Identify the blood parasite species.
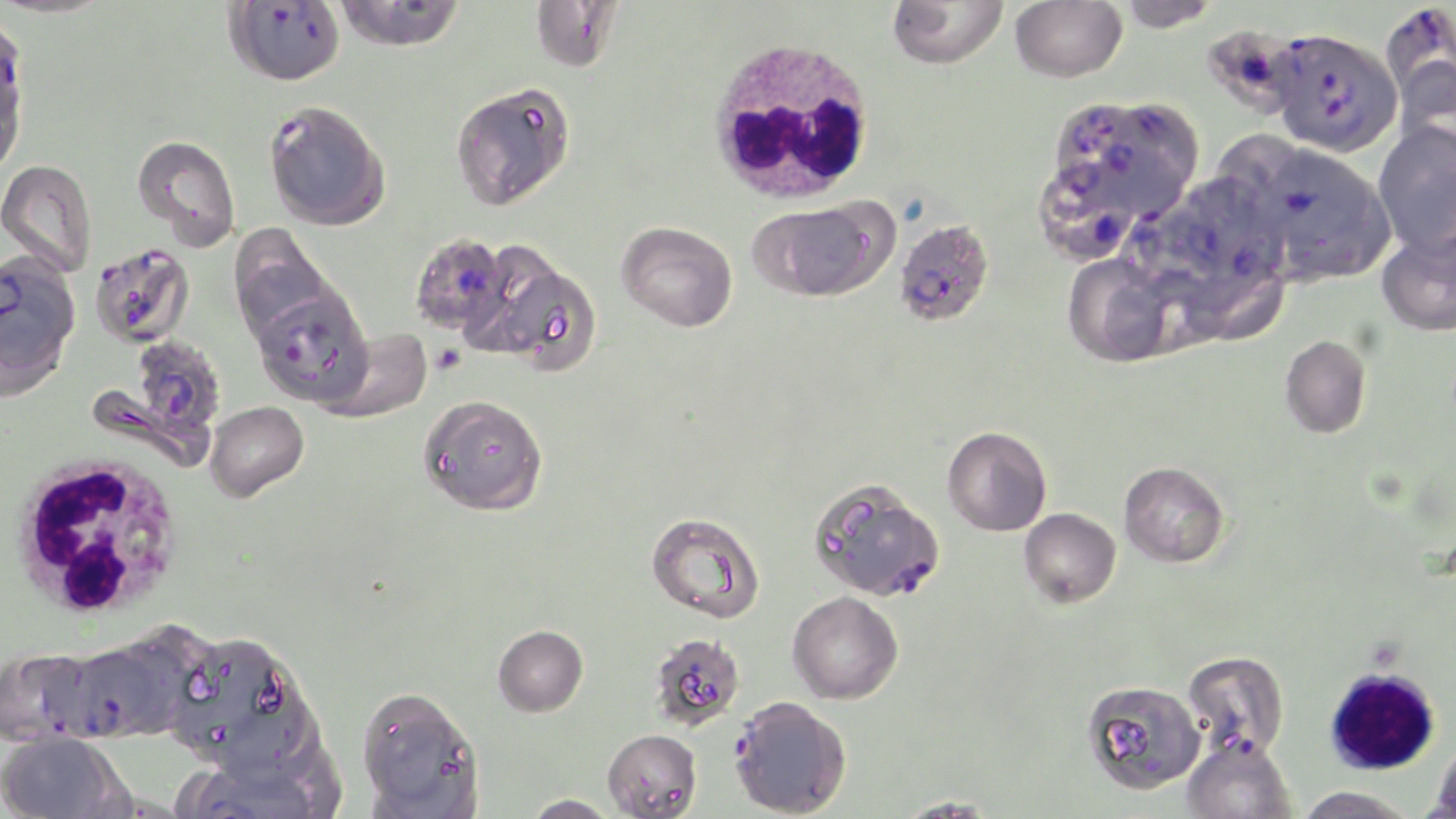
Plasmodium falciparum.

Approximate bounding boxes as (x1,y1)-(x2,y2) corner pairs in pixels. Plasmodium falciparum-infected red blood cell locations: (224,1)-(347,87), (1381,3)-(1456,128), (1201,24)-(1305,120), (1269,28)-(1402,157), (0,30)-(30,126), (1103,97)-(1207,189), (1054,99)-(1161,206), (263,100)-(390,231), (1266,150)-(1372,244), (1120,206)-(1222,302), (893,218)-(993,326), (409,232)-(512,336), (89,243)-(195,348), (0,253)-(81,394), (250,285)-(373,409), (128,337)-(227,443), (810,479)-(946,602), (63,642)-(177,742), (0,647)-(103,747), (1181,650)-(1289,759), (728,695)-(852,817). Platelet locations: (431,345)-(466,374). Uninfected red blood cell locations: (332,0)-(466,53), (531,0)-(624,72), (887,0)-(1009,70), (1010,0)-(1127,82), (1116,0)-(1221,31), (451,81)-(576,208), (1372,121)-(1456,255), (1220,129)-(1291,204), (132,134)-(241,251), (0,159)-(97,276), (751,201)-(886,299), (617,221)-(738,332), (229,224)-(334,342), (1376,226)-(1455,336), (1062,252)-(1179,367), (488,260)-(603,378), (1187,275)-(1297,350), (321,328)-(433,423), (1280,334)-(1372,438), (418,394)-(548,516), (205,401)-(309,502), (942,425)-(1052,536), (1118,460)-(1230,567), (1018,507)-(1121,608), (646,511)-(765,623), (787,591)-(903,704), (493,624)-(588,717), (167,632)-(313,775), (649,632)-(745,730), (1082,680)-(1205,794), (356,685)-(483,817), (602,728)-(702,818), (1,731)-(128,819), (1181,735)-(1297,819), (1430,739)-(1456,817), (1295,786)-(1418,819), (520,793)-(622,819), (893,796)-(1004,817). White blood cell locations: (702,36)-(878,207), (7,451)-(188,621), (1323,666)-(1439,776). Light microscopy. May-Grünwald-Giemsa-stained preparation. 1000x magnification. One field of a larger specimen. Image is 1456×819 pixels. Thin blood film.